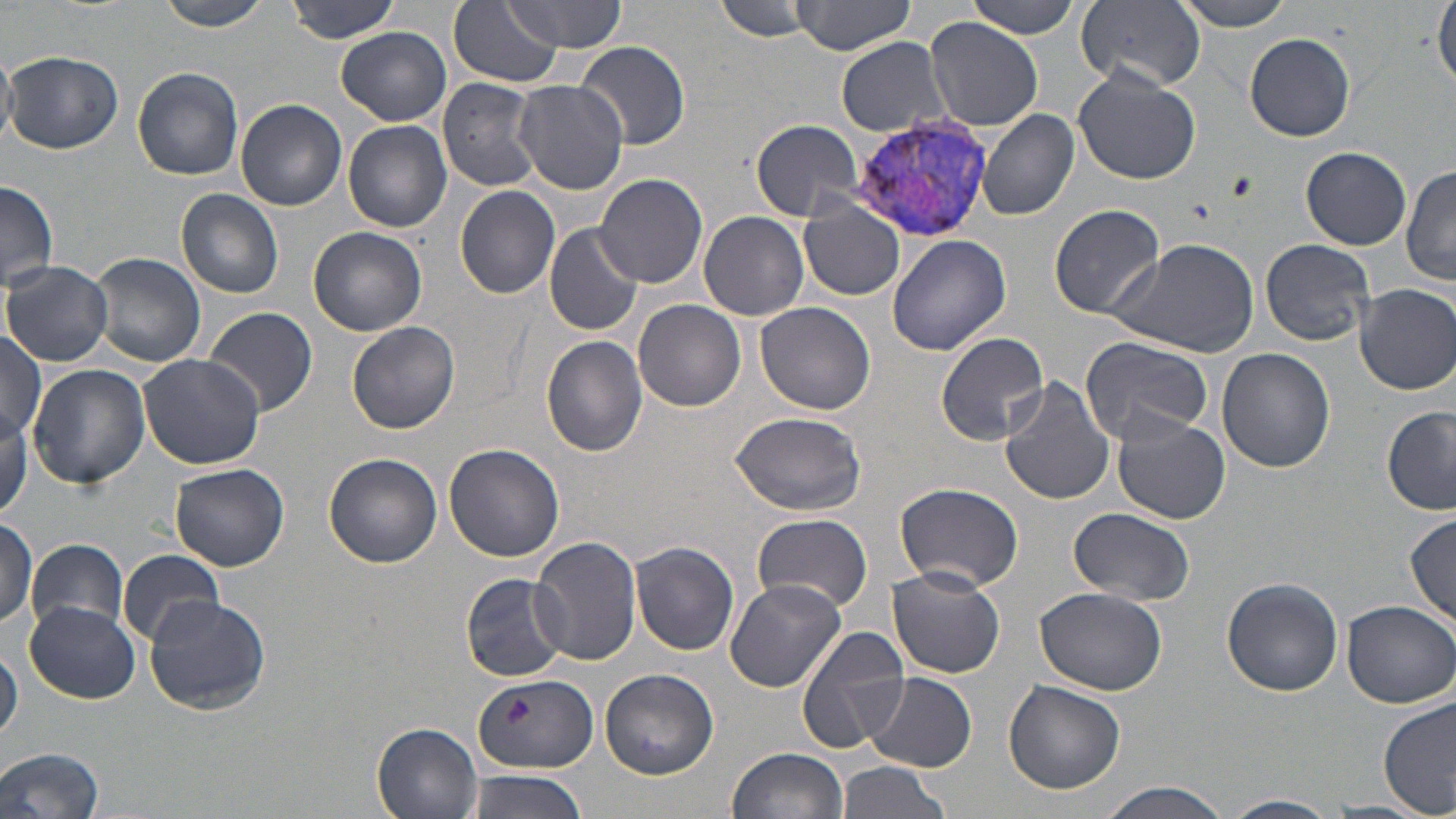

Summary:
  - Coordinate format: approximate bounding boxes as named x1/y1/x2/y2 corners in pixels
  - Platelet locations: (x1=1226, y1=170, x2=1257, y2=203), (x1=503, y1=697, x2=531, y2=728)
  - Uninfected red blood cell locations: (x1=152, y1=0, x2=280, y2=31), (x1=285, y1=0, x2=406, y2=44), (x1=507, y1=0, x2=627, y2=53), (x1=712, y1=0, x2=820, y2=42), (x1=790, y1=0, x2=917, y2=55), (x1=963, y1=0, x2=1086, y2=38), (x1=1165, y1=0, x2=1301, y2=31), (x1=1433, y1=0, x2=1456, y2=91), (x1=449, y1=2, x2=561, y2=88), (x1=1072, y1=2, x2=1206, y2=93), (x1=923, y1=17, x2=1044, y2=131), (x1=337, y1=27, x2=451, y2=126), (x1=1244, y1=33, x2=1356, y2=142), (x1=573, y1=39, x2=691, y2=149), (x1=836, y1=39, x2=954, y2=136), (x1=0, y1=49, x2=16, y2=146), (x1=4, y1=51, x2=123, y2=155), (x1=1072, y1=65, x2=1202, y2=184), (x1=131, y1=66, x2=244, y2=180), (x1=437, y1=77, x2=545, y2=191), (x1=513, y1=80, x2=628, y2=194), (x1=236, y1=99, x2=347, y2=211), (x1=977, y1=109, x2=1080, y2=221), (x1=750, y1=117, x2=866, y2=221), (x1=344, y1=120, x2=451, y2=234), (x1=1300, y1=147, x2=1412, y2=250), (x1=1402, y1=164, x2=1456, y2=286), (x1=595, y1=173, x2=708, y2=287), (x1=0, y1=180, x2=58, y2=291), (x1=455, y1=184, x2=561, y2=299), (x1=176, y1=189, x2=285, y2=298), (x1=551, y1=190, x2=697, y2=327), (x1=798, y1=202, x2=905, y2=301), (x1=1049, y1=205, x2=1166, y2=318), (x1=698, y1=211, x2=808, y2=320), (x1=543, y1=222, x2=644, y2=337), (x1=308, y1=226, x2=427, y2=336), (x1=886, y1=235, x2=1010, y2=356), (x1=1260, y1=237, x2=1375, y2=347), (x1=1107, y1=238, x2=1260, y2=357), (x1=90, y1=252, x2=205, y2=367), (x1=3, y1=261, x2=114, y2=366), (x1=1354, y1=283, x2=1456, y2=394), (x1=633, y1=299, x2=747, y2=412), (x1=755, y1=301, x2=876, y2=416), (x1=203, y1=306, x2=318, y2=417), (x1=346, y1=321, x2=459, y2=435), (x1=0, y1=329, x2=47, y2=445), (x1=936, y1=330, x2=1052, y2=445), (x1=542, y1=336, x2=649, y2=455), (x1=1081, y1=336, x2=1212, y2=443), (x1=1216, y1=348, x2=1335, y2=472), (x1=138, y1=353, x2=265, y2=469), (x1=27, y1=364, x2=149, y2=489), (x1=998, y1=377, x2=1116, y2=506), (x1=1383, y1=405, x2=1456, y2=516), (x1=729, y1=411, x2=868, y2=516), (x1=1111, y1=412, x2=1231, y2=523), (x1=445, y1=443, x2=564, y2=563), (x1=324, y1=454, x2=443, y2=569), (x1=170, y1=462, x2=289, y2=570), (x1=894, y1=481, x2=1024, y2=592), (x1=1066, y1=508, x2=1197, y2=606), (x1=1405, y1=512, x2=1456, y2=626), (x1=752, y1=515, x2=874, y2=615), (x1=0, y1=516, x2=37, y2=630), (x1=532, y1=537, x2=642, y2=667), (x1=27, y1=540, x2=128, y2=637), (x1=631, y1=542, x2=740, y2=655), (x1=118, y1=548, x2=224, y2=646), (x1=885, y1=567, x2=1005, y2=678), (x1=460, y1=572, x2=571, y2=680), (x1=1221, y1=576, x2=1344, y2=696), (x1=724, y1=579, x2=847, y2=693), (x1=1035, y1=586, x2=1167, y2=694), (x1=143, y1=596, x2=271, y2=716), (x1=1338, y1=599, x2=1454, y2=710), (x1=23, y1=601, x2=140, y2=704), (x1=796, y1=626, x2=911, y2=753), (x1=0, y1=644, x2=22, y2=746), (x1=600, y1=668, x2=718, y2=779), (x1=865, y1=672, x2=976, y2=771), (x1=473, y1=676, x2=599, y2=772), (x1=1002, y1=680, x2=1126, y2=794), (x1=1379, y1=696, x2=1456, y2=817), (x1=371, y1=719, x2=484, y2=818), (x1=725, y1=747, x2=849, y2=819), (x1=0, y1=748, x2=107, y2=819), (x1=834, y1=762, x2=950, y2=819), (x1=463, y1=769, x2=590, y2=819), (x1=1091, y1=783, x2=1238, y2=819), (x1=1222, y1=795, x2=1340, y2=818)
  - Plasmodium vivax-infected red blood cell locations: (x1=849, y1=116, x2=1006, y2=242)
  - Slide-level diagnosis: Plasmodium vivax
  - Modality: light microscopy
  - Stain: May-Grünwald-Giemsa
  - Preparation: thin blood smear
  - Field of view: one of a larger specimen
  - Magnification: 1000x
  - Image size: 1456×819 pixels